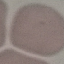
Summary:
  - Malaria status: uninfected
  - Capture: smartphone through the microscope eyepiece
  - Stain: Giemsa
  - Preparation: thin blood film
  - Image type: cell patch, automatically extracted from a larger field of view and resized to 64 × 64 pixels